Locate platelets.
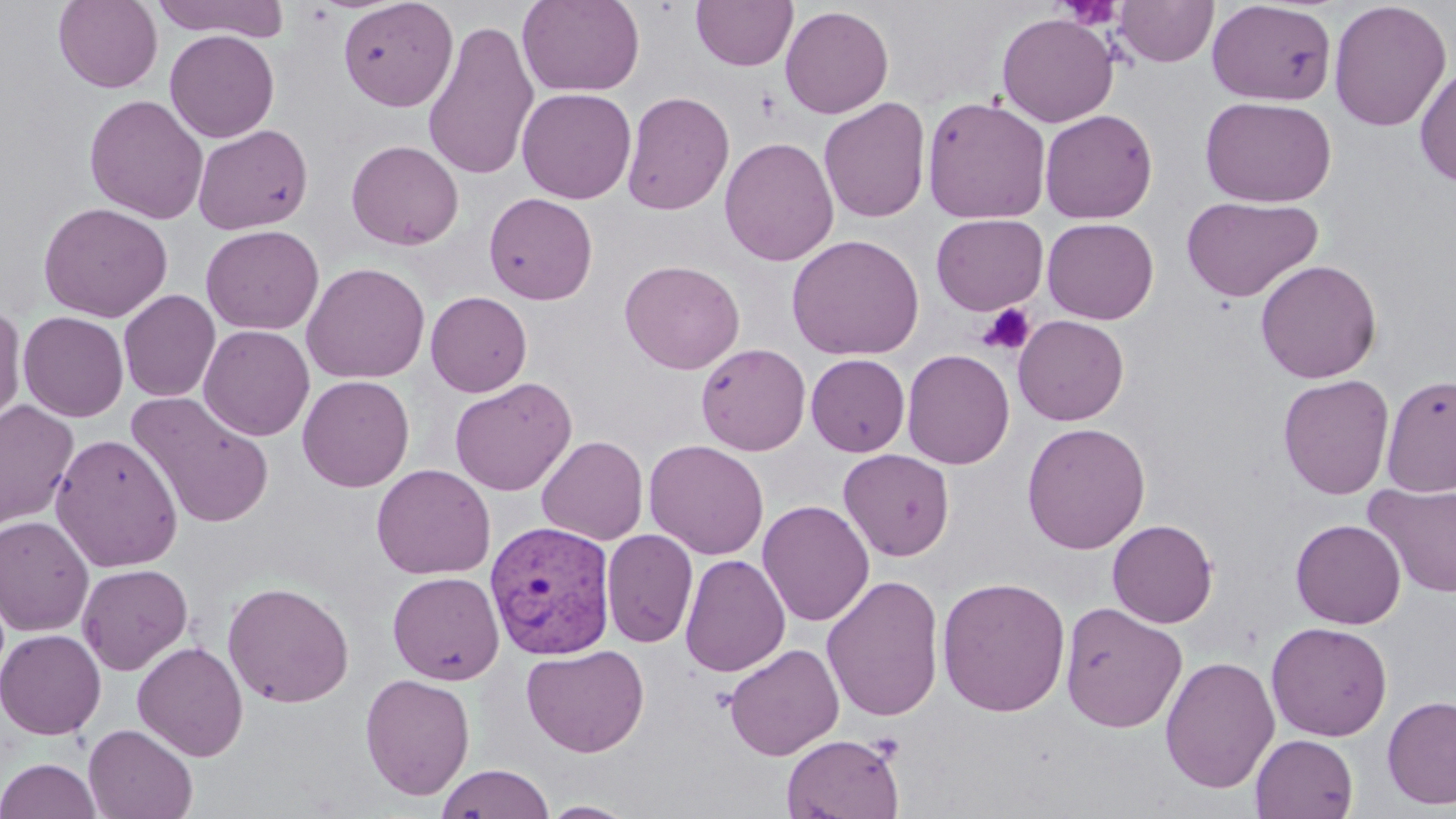
Approximate bounding boxes as (x1, y1, x2, y2) in pixels.
Platelets: (1059, 1, 1123, 30), (976, 303, 1036, 356).

Plasmodium vivax-infected red blood cell locations: (484, 519, 617, 659). Uninfected red blood cell locations: (52, 0, 164, 93), (148, 0, 293, 41), (338, 0, 458, 111), (517, 0, 645, 97), (691, 0, 798, 71), (1113, 0, 1218, 67), (1328, 0, 1452, 132), (1207, 2, 1337, 106), (780, 5, 894, 118), (996, 13, 1119, 127), (423, 20, 540, 181), (164, 29, 280, 143), (1415, 64, 1456, 188), (517, 87, 637, 204), (621, 90, 735, 216), (84, 94, 209, 224), (921, 96, 1052, 224), (1200, 96, 1337, 208), (819, 97, 931, 223), (1040, 109, 1158, 224), (193, 124, 313, 234), (719, 136, 839, 267), (346, 139, 464, 250), (483, 192, 598, 305), (1181, 195, 1323, 303), (38, 201, 173, 322), (930, 214, 1048, 314), (1042, 217, 1159, 324), (200, 225, 323, 335), (786, 234, 924, 361), (619, 259, 744, 374), (1255, 259, 1382, 383), (300, 262, 431, 384), (118, 289, 221, 402), (425, 290, 532, 397), (0, 303, 27, 431), (18, 311, 129, 422), (1012, 314, 1129, 426), (198, 324, 315, 441), (695, 343, 811, 455), (902, 349, 1015, 469), (806, 353, 911, 456), (1277, 374, 1395, 500), (1381, 374, 1456, 497), (297, 375, 415, 491), (449, 377, 577, 496), (126, 391, 274, 528), (0, 400, 79, 530), (1021, 421, 1151, 554), (50, 433, 184, 572), (537, 435, 649, 545), (644, 439, 770, 560), (838, 448, 955, 561), (371, 464, 495, 580), (1363, 482, 1456, 598), (757, 499, 874, 627), (0, 515, 94, 636), (1291, 518, 1406, 629), (1107, 519, 1218, 628), (601, 529, 699, 648), (679, 554, 790, 677), (77, 563, 193, 675), (387, 571, 504, 684), (822, 574, 945, 722), (936, 575, 1072, 717), (222, 581, 355, 708), (1060, 601, 1188, 732), (1266, 621, 1392, 741), (0, 628, 106, 740), (132, 641, 248, 761), (522, 643, 650, 757), (724, 643, 844, 760), (1159, 655, 1280, 793), (359, 672, 475, 800), (1382, 695, 1456, 810), (83, 724, 198, 818), (781, 733, 906, 818), (1250, 734, 1358, 819), (0, 757, 101, 818), (435, 764, 555, 819), (539, 800, 640, 818). Slide-level diagnosis: Plasmodium vivax. One field of a larger specimen. May-Grünwald-Giemsa stain. Image is 1456×819 pixels. Optical microscopy. 1000x magnification. Thin blood film.